Comment on the morphology of the erythrocytes.
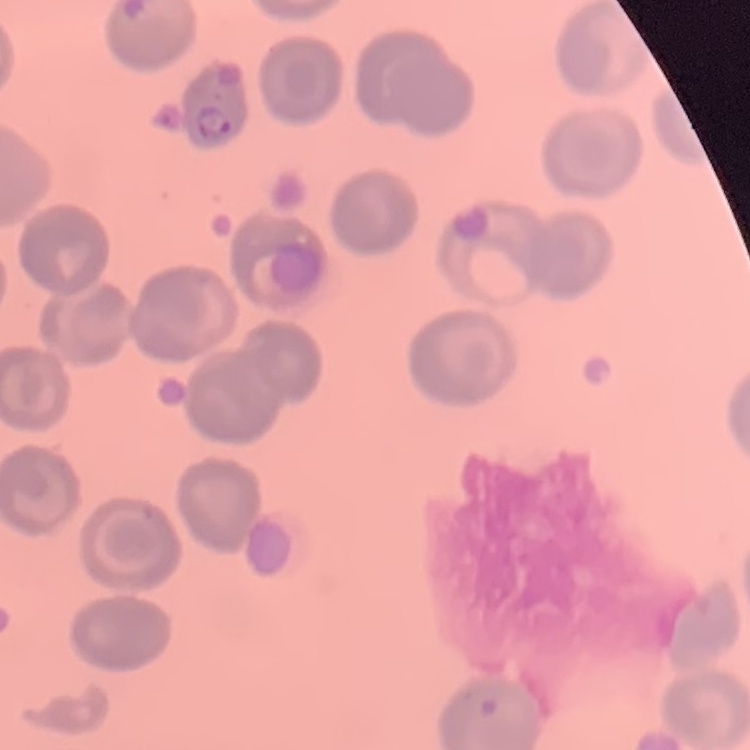

They show no rouleaux formation.

Summary:
  - Preparation: thin blood film
  - Image type: square crop of a larger photomicrograph
  - Stain: Field's or Giemsa